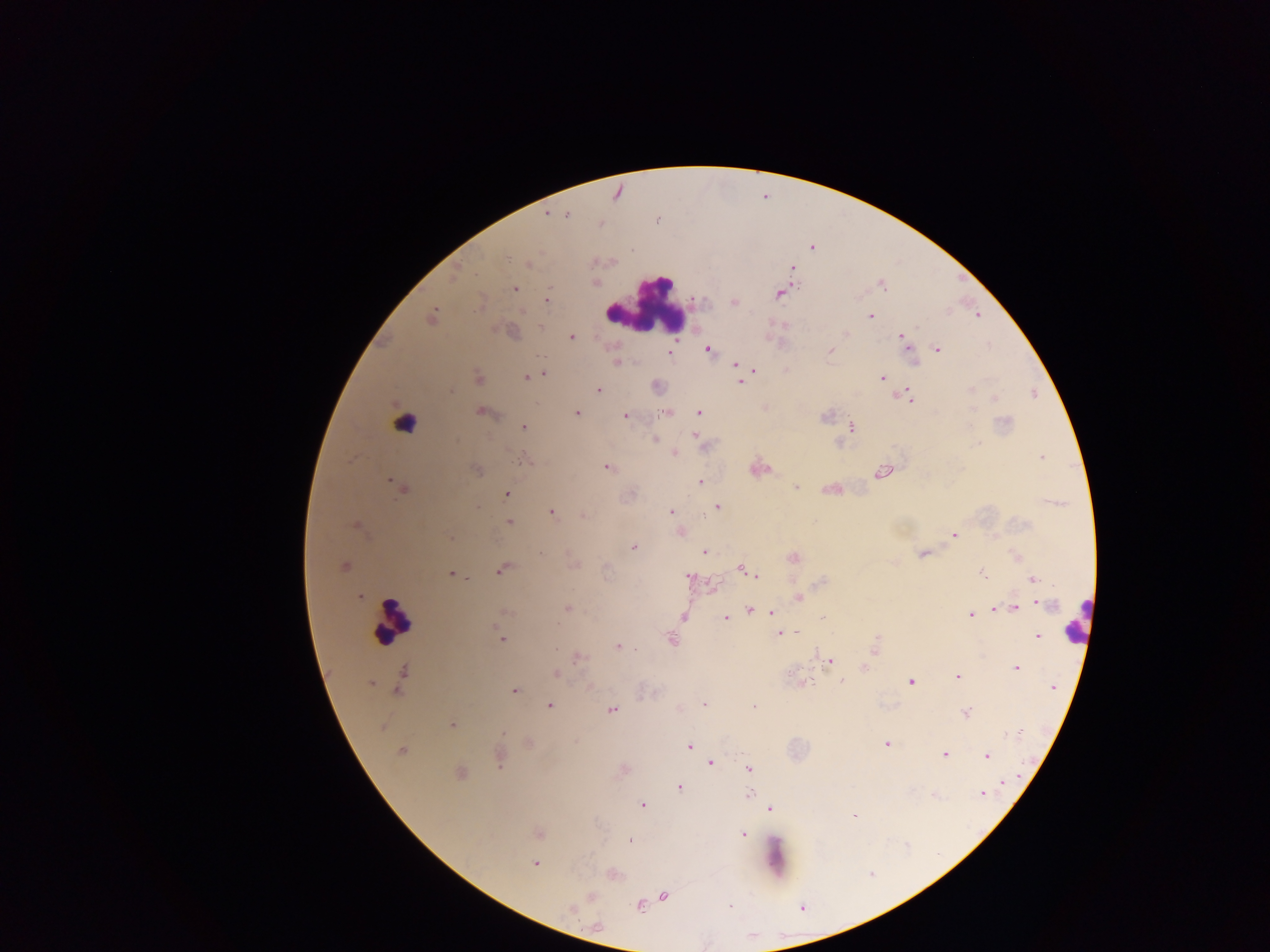

image size = 1270×952 pixels
field of view = single
capture = mobile-phone photograph through a microscope
country = Ghana
preparation = thick blood film
Plasmodium parasite locations = approximate centers as x y in pixels: 548 213; 567 215; 657 221; 505 256; 529 263; 792 268; 454 276; 882 286; 515 289; 778 294; 546 300; 734 302; 524 312; 431 315; 978 315; 870 316; 541 327; 847 333; 901 336; 572 337; 937 349; 708 350; 830 350; 669 353; 616 363; 737 365; 753 369; 543 374; 527 377; 478 378; 882 378; 741 382; 970 389; 598 390; 450 392; 908 396; 995 397; 974 411; 483 413; 576 413; 699 413; 667 414; 625 416; 1005 422; 524 427; 851 428; 695 435; 655 440; 674 454; 1040 457; 524 460; 606 467; 477 470; 882 473; 390 480; 700 483; 795 487; 402 490; 507 494; 718 506; 477 508; 551 512; 671 512; 583 516; 509 522; 356 524; 681 532; 955 535; 633 547; 704 552; 922 554; 793 558; 345 566; 501 570; 743 570; 982 572; 452 574; 752 574; 688 576; 1033 579; 359 596; 799 598; 1046 604; 568 609; 996 609; 1015 609; 750 610; 505 611; 772 612; 970 614; 684 617; 725 617; 823 618; 557 626; 786 632; 797 632; 780 634; 1038 636; 500 638; 671 640; 618 647; 635 649; 875 650; 579 658; 830 660; 864 668; 1016 668; 403 672; 556 673; 957 676; 841 681; 910 682; 371 683; 1053 687; 515 690; 397 691; 704 704; 549 706; 755 706; 612 710; 966 713; 452 725; 504 733; 1016 733; 886 744; 689 746; 401 752; 944 754; 987 756; 710 762; 500 763; 748 769; 461 772; 1004 782; 679 787; 982 793; 749 795; 642 805; 770 809; 854 816; 538 833; 743 834; 629 840; 535 864; 590 896; 664 896; 639 905; 730 907; 570 909; 597 926
leukocyte locations = approximate centers as x y in pixels: 646 306; 404 422; 393 619; 1078 619